Locate every blood parasite and identify its species.
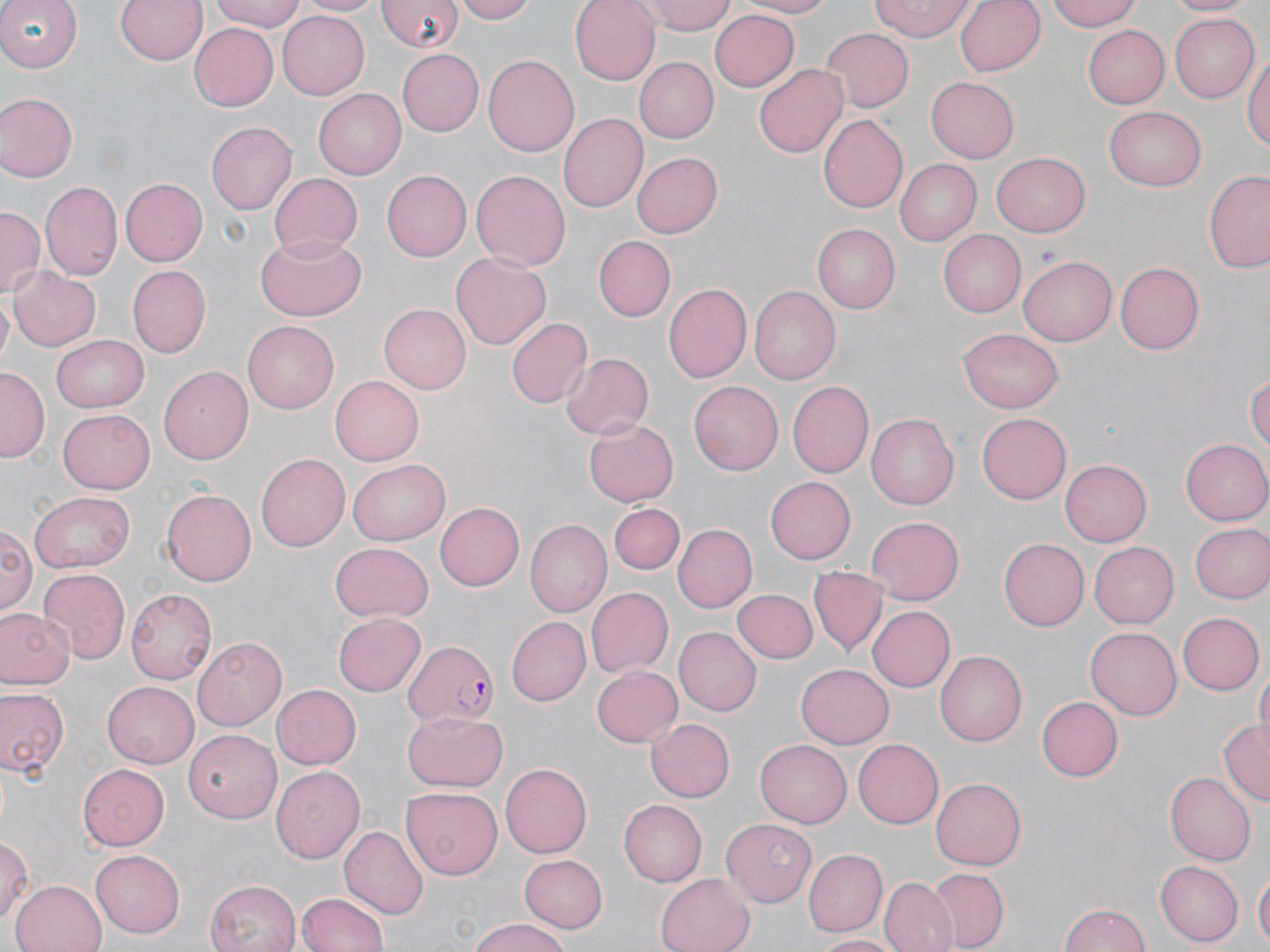

Approximate bounding boxes as (x1, y1, x2, y2) in pixels.
Plasmodium falciparum-infected red blood cells: (401, 640, 500, 729).
No Plasmodium ovale, Plasmodium malariae, Plasmodium vivax, Babesia divergens, or Trypanosoma brucei observed.

Uninfected red blood cell locations: (115, 0, 207, 68), (207, 0, 307, 31), (295, 0, 385, 17), (379, 0, 460, 54), (455, 0, 539, 23), (568, 0, 660, 84), (647, 0, 733, 34), (733, 0, 842, 17), (868, 0, 974, 42), (953, 0, 1045, 77), (1045, 0, 1143, 32), (1166, 0, 1254, 17), (0, 1, 81, 72), (709, 8, 799, 91), (276, 10, 369, 100), (1168, 13, 1258, 102), (189, 26, 277, 111), (818, 27, 912, 114), (1084, 27, 1168, 108), (395, 49, 483, 136), (1243, 50, 1269, 158), (483, 54, 580, 158), (634, 57, 717, 143), (753, 63, 847, 158), (926, 76, 1020, 162), (312, 89, 405, 179), (0, 92, 77, 182), (1106, 105, 1206, 190), (558, 113, 650, 213), (818, 115, 909, 214), (206, 121, 298, 215), (631, 152, 722, 238), (992, 152, 1090, 235), (896, 159, 982, 245), (1204, 164, 1270, 275), (381, 169, 471, 261), (471, 170, 571, 271), (268, 172, 363, 257), (120, 178, 207, 266), (43, 180, 124, 280), (0, 206, 43, 299), (813, 225, 901, 312), (938, 230, 1026, 318), (254, 232, 366, 319), (592, 235, 674, 321), (451, 251, 550, 347), (1020, 257, 1117, 345), (1116, 261, 1204, 355), (126, 265, 209, 359), (10, 268, 99, 351), (661, 281, 752, 383), (749, 285, 841, 385), (379, 304, 472, 395), (505, 317, 591, 408), (244, 321, 339, 413), (956, 329, 1062, 412), (50, 333, 148, 413), (561, 352, 654, 440), (159, 367, 253, 465), (0, 368, 48, 459), (1247, 372, 1270, 460), (329, 375, 425, 465), (689, 379, 782, 472), (787, 381, 873, 478), (57, 408, 154, 493), (977, 411, 1070, 501), (868, 412, 958, 507), (584, 420, 678, 506), (1181, 440, 1269, 524), (257, 452, 351, 553), (349, 458, 450, 544), (1059, 459, 1152, 546), (766, 477, 857, 563), (161, 488, 256, 586), (29, 490, 135, 571), (436, 501, 526, 591), (610, 503, 684, 575), (864, 516, 964, 604), (523, 521, 610, 618), (1, 522, 35, 620), (1188, 523, 1270, 602), (673, 524, 756, 612), (997, 539, 1089, 631), (1088, 540, 1178, 629), (327, 544, 434, 625), (37, 567, 131, 661), (808, 567, 888, 656), (584, 587, 672, 677), (125, 588, 217, 683), (732, 589, 816, 662), (868, 605, 954, 692), (0, 607, 74, 689), (1178, 613, 1263, 694), (333, 614, 426, 696), (503, 615, 589, 706), (1086, 628, 1181, 719), (675, 629, 761, 715), (193, 637, 289, 732), (934, 651, 1025, 746), (796, 662, 894, 747), (590, 664, 682, 746), (1256, 666, 1269, 748), (103, 681, 199, 766), (271, 685, 361, 769), (0, 687, 69, 778), (1038, 696, 1125, 781), (403, 711, 507, 792), (646, 716, 734, 801), (1219, 718, 1269, 806), (182, 728, 282, 818), (851, 739, 942, 828), (754, 740, 849, 827), (77, 762, 169, 849), (500, 763, 591, 857), (271, 764, 364, 864), (1166, 772, 1255, 865), (930, 777, 1025, 870), (400, 785, 505, 879), (619, 799, 706, 886), (722, 818, 818, 905), (339, 827, 428, 917), (0, 833, 31, 930), (805, 849, 887, 936), (89, 850, 185, 938), (519, 854, 608, 932), (1154, 860, 1242, 946), (924, 868, 1007, 951), (1253, 870, 1270, 949), (655, 874, 754, 952), (880, 876, 957, 952), (9, 879, 106, 952), (204, 879, 300, 952), (295, 890, 389, 952), (1058, 904, 1151, 952), (463, 919, 576, 952), (807, 933, 899, 950). Slide-level diagnosis: Plasmodium falciparum. Captured at 1000x magnification. May-Grünwald-Giemsa stain. Optical microscopy. Thin blood smear. Single field of view. Image is 1270×952 pixels.